Assess this cell for malaria.
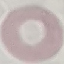
It is uninfected.

image type = cell patch, automatically extracted from a larger field of view and resized to 64 × 64 pixels
stain = Giemsa
capture = smartphone camera at the microscope eyepiece
preparation = thin blood smear